Locate and identify every blood parasite.
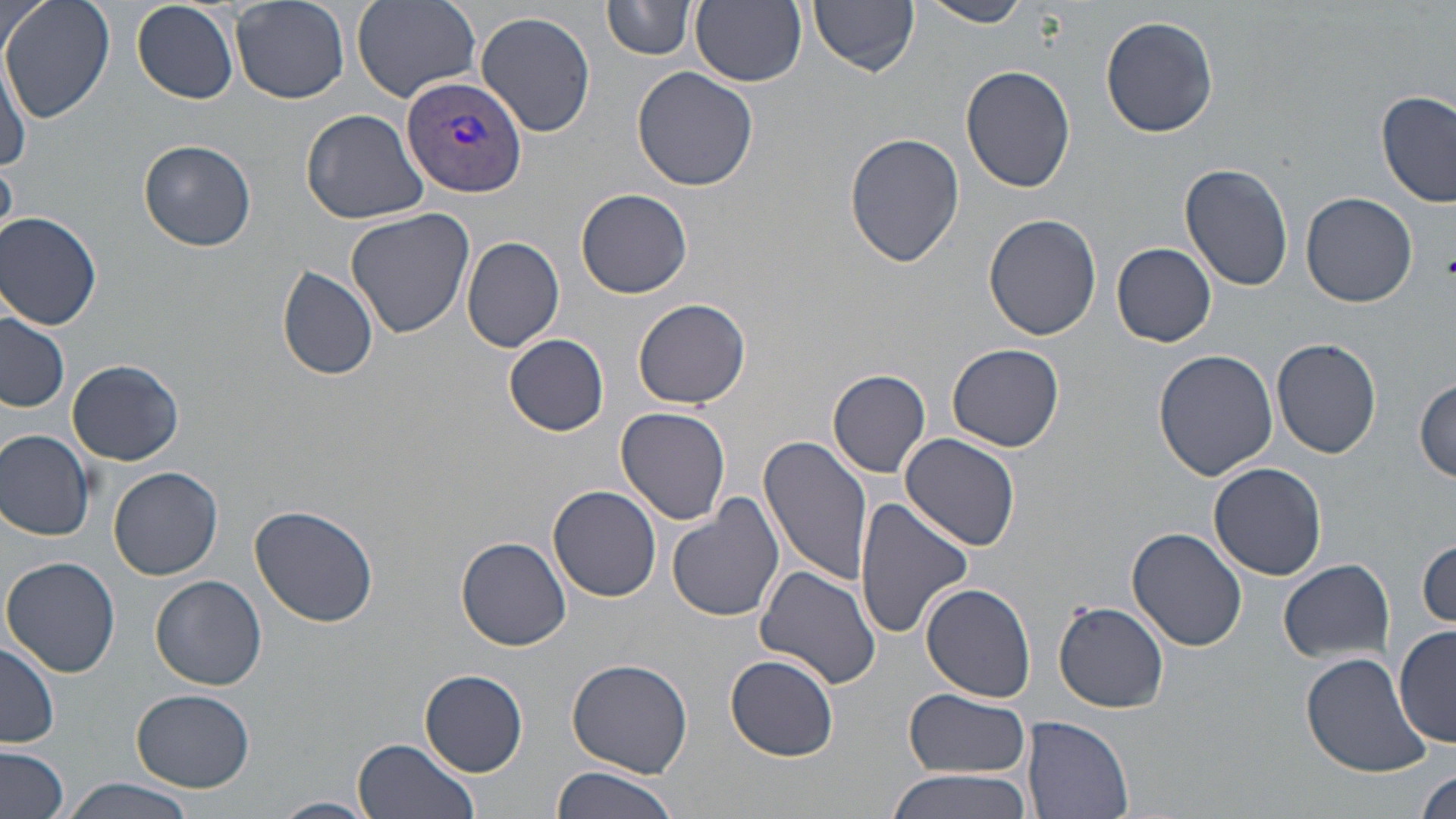
Approximate bounding boxes as named x1/y1/x2/y2 corners in pixels.
Plasmodium vivax-infected red blood cells: (x1=400, y1=74, x2=527, y2=200).
No Plasmodium falciparum, Plasmodium ovale, Plasmodium malariae, Babesia divergens, or Trypanosoma brucei observed.

Summary:
  - Uninfected red blood cell locations: (x1=2, y1=0, x2=114, y2=122), (x1=230, y1=0, x2=350, y2=104), (x1=353, y1=0, x2=481, y2=102), (x1=598, y1=0, x2=779, y2=68), (x1=603, y1=0, x2=696, y2=60), (x1=809, y1=0, x2=920, y2=74), (x1=917, y1=0, x2=1035, y2=27), (x1=691, y1=1, x2=807, y2=88), (x1=132, y1=2, x2=240, y2=104), (x1=476, y1=10, x2=597, y2=138), (x1=1100, y1=15, x2=1219, y2=138), (x1=1, y1=57, x2=30, y2=174), (x1=962, y1=64, x2=1077, y2=193), (x1=632, y1=66, x2=760, y2=192), (x1=1377, y1=90, x2=1456, y2=209), (x1=302, y1=108, x2=430, y2=223), (x1=844, y1=132, x2=964, y2=269), (x1=139, y1=140, x2=256, y2=251), (x1=1178, y1=162, x2=1295, y2=293), (x1=576, y1=187, x2=692, y2=298), (x1=1301, y1=192, x2=1418, y2=308), (x1=346, y1=209, x2=476, y2=338), (x1=0, y1=212, x2=103, y2=331), (x1=984, y1=213, x2=1102, y2=341), (x1=461, y1=236, x2=566, y2=352), (x1=1112, y1=241, x2=1215, y2=347), (x1=276, y1=266, x2=379, y2=381), (x1=634, y1=297, x2=751, y2=408), (x1=0, y1=308, x2=71, y2=412), (x1=504, y1=333, x2=611, y2=436), (x1=1271, y1=338, x2=1383, y2=460), (x1=948, y1=344, x2=1064, y2=451), (x1=1152, y1=348, x2=1276, y2=481), (x1=68, y1=359, x2=184, y2=465), (x1=827, y1=368, x2=933, y2=477), (x1=1414, y1=380, x2=1455, y2=483), (x1=616, y1=407, x2=732, y2=524), (x1=1, y1=430, x2=97, y2=541), (x1=757, y1=433, x2=871, y2=586), (x1=899, y1=433, x2=1021, y2=552), (x1=1209, y1=461, x2=1327, y2=580), (x1=111, y1=468, x2=223, y2=580), (x1=549, y1=485, x2=663, y2=602), (x1=666, y1=494, x2=785, y2=623), (x1=853, y1=497, x2=974, y2=640), (x1=250, y1=504, x2=380, y2=628), (x1=1127, y1=527, x2=1248, y2=650), (x1=455, y1=535, x2=572, y2=650), (x1=1416, y1=537, x2=1454, y2=628), (x1=3, y1=556, x2=122, y2=678), (x1=1279, y1=558, x2=1395, y2=666), (x1=754, y1=565, x2=881, y2=689), (x1=152, y1=576, x2=267, y2=690), (x1=921, y1=582, x2=1036, y2=702), (x1=1054, y1=601, x2=1172, y2=713), (x1=1393, y1=625, x2=1455, y2=750), (x1=1, y1=639, x2=61, y2=748), (x1=1301, y1=652, x2=1431, y2=777), (x1=725, y1=654, x2=840, y2=760), (x1=566, y1=657, x2=694, y2=777), (x1=420, y1=669, x2=528, y2=776), (x1=131, y1=688, x2=256, y2=792), (x1=905, y1=688, x2=1029, y2=779), (x1=1022, y1=716, x2=1136, y2=819), (x1=354, y1=736, x2=479, y2=819), (x1=0, y1=746, x2=71, y2=819), (x1=550, y1=765, x2=682, y2=819), (x1=885, y1=767, x2=1037, y2=819), (x1=1415, y1=768, x2=1454, y2=817), (x1=57, y1=779, x2=200, y2=819), (x1=269, y1=796, x2=376, y2=819)
  - Platelet locations: (x1=1443, y1=250, x2=1456, y2=280)
  - Slide-level diagnosis: Plasmodium vivax
  - Image size: 1456×819 pixels
  - Preparation: thin blood film
  - Magnification: 1000x
  - Modality: light microscopy
  - Stain: May-Grünwald-Giemsa
  - Field of view: single